State which parasite is depicted.
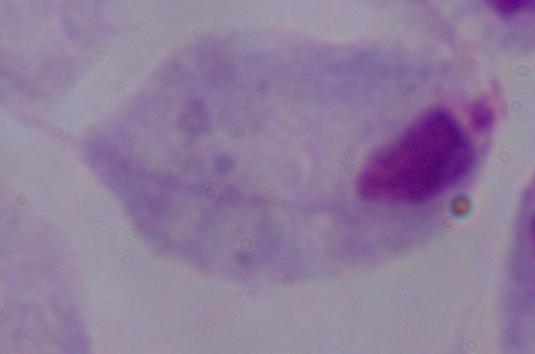

A trichomonad.

Micrograph. Captured at 1000x magnification.